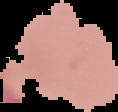

{
  "result": "no malaria parasites detected",
  "preparation": "thin blood smear",
  "image_type": "segmented cell region with the area outside set to black",
  "image_size": "118×112 pixels"
}